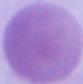

Summary:
  - Identification: erythrocyte
  - Modality: photomicrograph
  - Magnification: 1000x